Assess this cell for malaria.
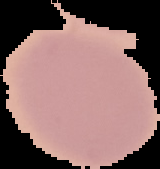
Uninfected.

Image is 160×169 pixels. From a thin blood film. Cell region segmented out of the field of view; the surrounding area is masked to black.